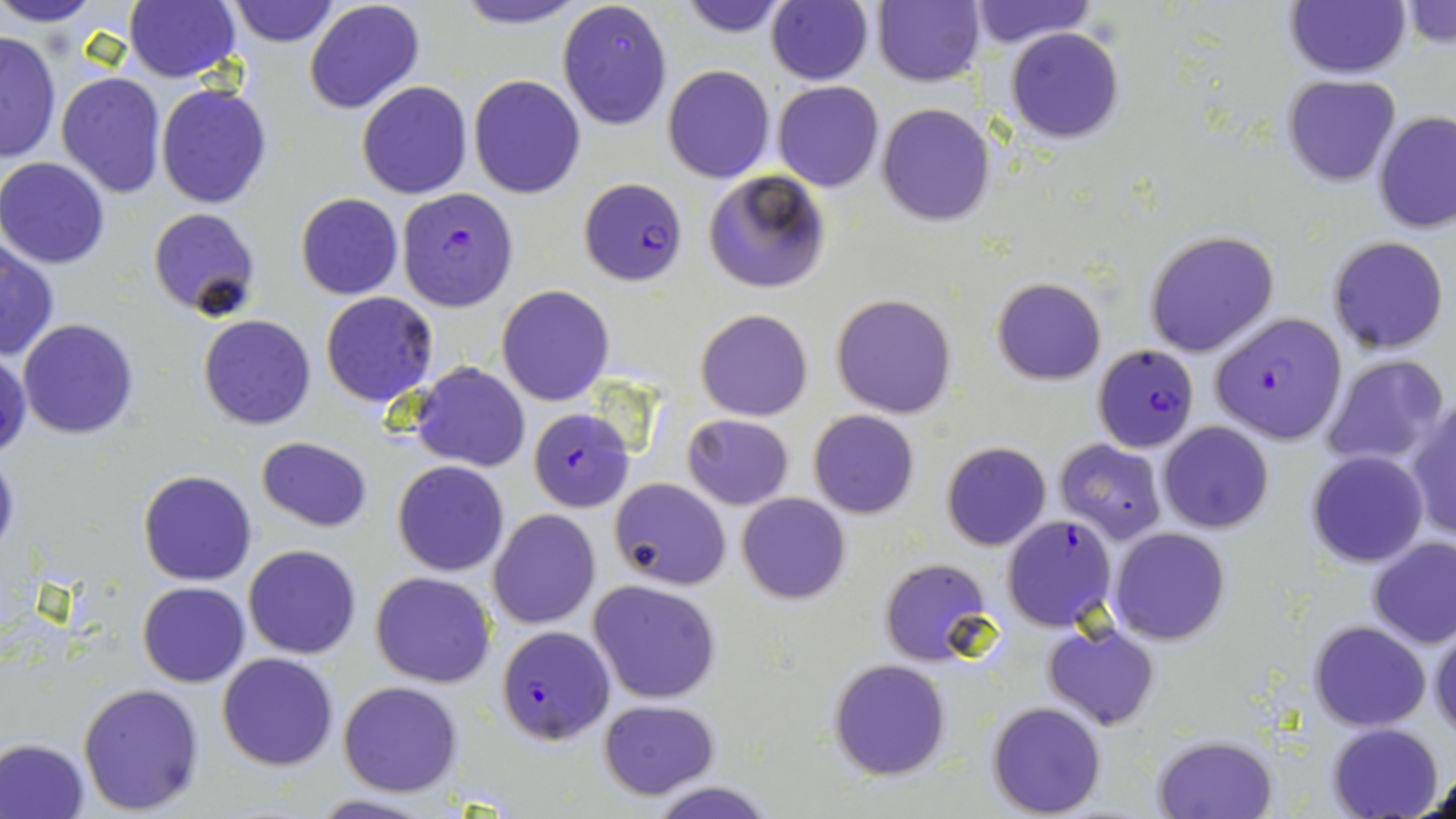
Approximate bounding boxes as (x1,y1)-(x2,y2) corner pairs in pixels. Plasmodium falciparum-infected red blood cell locations: (580,177)-(688,285), (396,187)-(519,312), (1211,312)-(1348,446), (1092,344)-(1200,474), (527,407)-(634,512), (999,514)-(1118,633), (495,625)-(614,745). Uninfected red blood cell locations: (0,0)-(105,27), (123,0)-(241,83), (450,0)-(589,30), (556,0)-(672,131), (675,0)-(795,37), (228,1)-(341,48), (304,1)-(426,116), (765,1)-(874,85), (871,1)-(986,87), (968,1)-(1093,50), (1285,1)-(1411,79), (1401,2)-(1456,51), (1006,27)-(1125,145), (0,29)-(61,164), (663,65)-(774,183), (55,72)-(168,198), (1281,74)-(1401,187), (469,75)-(586,199), (772,80)-(885,192), (355,81)-(474,199), (155,84)-(272,210), (877,103)-(995,225), (1374,110)-(1456,233), (0,157)-(110,269), (703,170)-(831,294), (296,193)-(403,300), (147,207)-(261,319), (1143,229)-(1280,358), (1326,235)-(1450,355), (0,236)-(57,361), (991,279)-(1105,385), (497,284)-(613,405), (320,292)-(438,407), (831,294)-(957,419), (695,308)-(813,422), (197,314)-(317,431), (18,318)-(141,440), (0,346)-(31,459), (1320,354)-(1451,469), (410,362)-(530,471), (1407,399)-(1456,542), (808,409)-(920,519), (682,414)-(794,510), (1158,421)-(1273,534), (256,437)-(370,532), (1055,439)-(1167,546), (941,442)-(1052,551), (0,445)-(20,563), (1307,450)-(1429,568), (392,460)-(508,575), (137,469)-(257,585), (609,477)-(731,590), (736,492)-(851,605), (488,509)-(601,629), (1108,526)-(1232,646), (1366,537)-(1456,650), (242,544)-(362,659), (879,558)-(994,667), (370,572)-(496,688), (588,579)-(724,704), (137,581)-(250,686), (1309,620)-(1431,731), (1043,623)-(1160,731), (1429,626)-(1456,741), (216,652)-(340,770), (828,659)-(951,781), (337,680)-(465,797), (77,682)-(204,815), (598,699)-(720,801), (988,701)-(1107,817), (1327,722)-(1444,819), (1154,734)-(1277,818), (0,737)-(91,818), (1417,767)-(1455,818), (647,781)-(777,818), (307,792)-(437,819). Slide-level diagnosis: Plasmodium falciparum. May-Grünwald-Giemsa stain. 1000x magnification. Light microscopy. Thin blood film. Image is 1456×819 pixels. One field of a larger specimen.